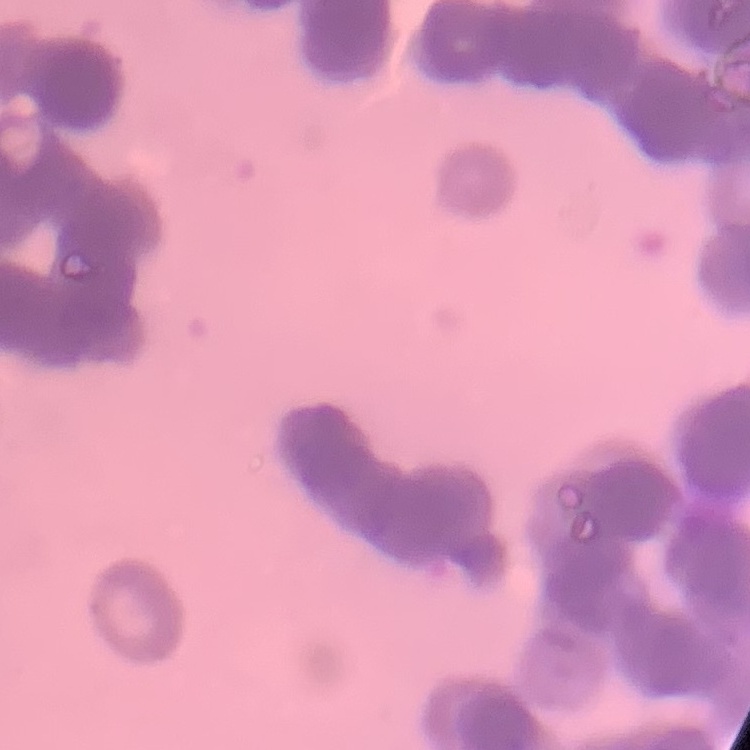

Summary:
  - Red blood cell morphology: rouleaux formation
  - Preparation: thin blood film
  - Stain: Field's or Giemsa
  - Image type: one tile cut from a larger photomicrograph